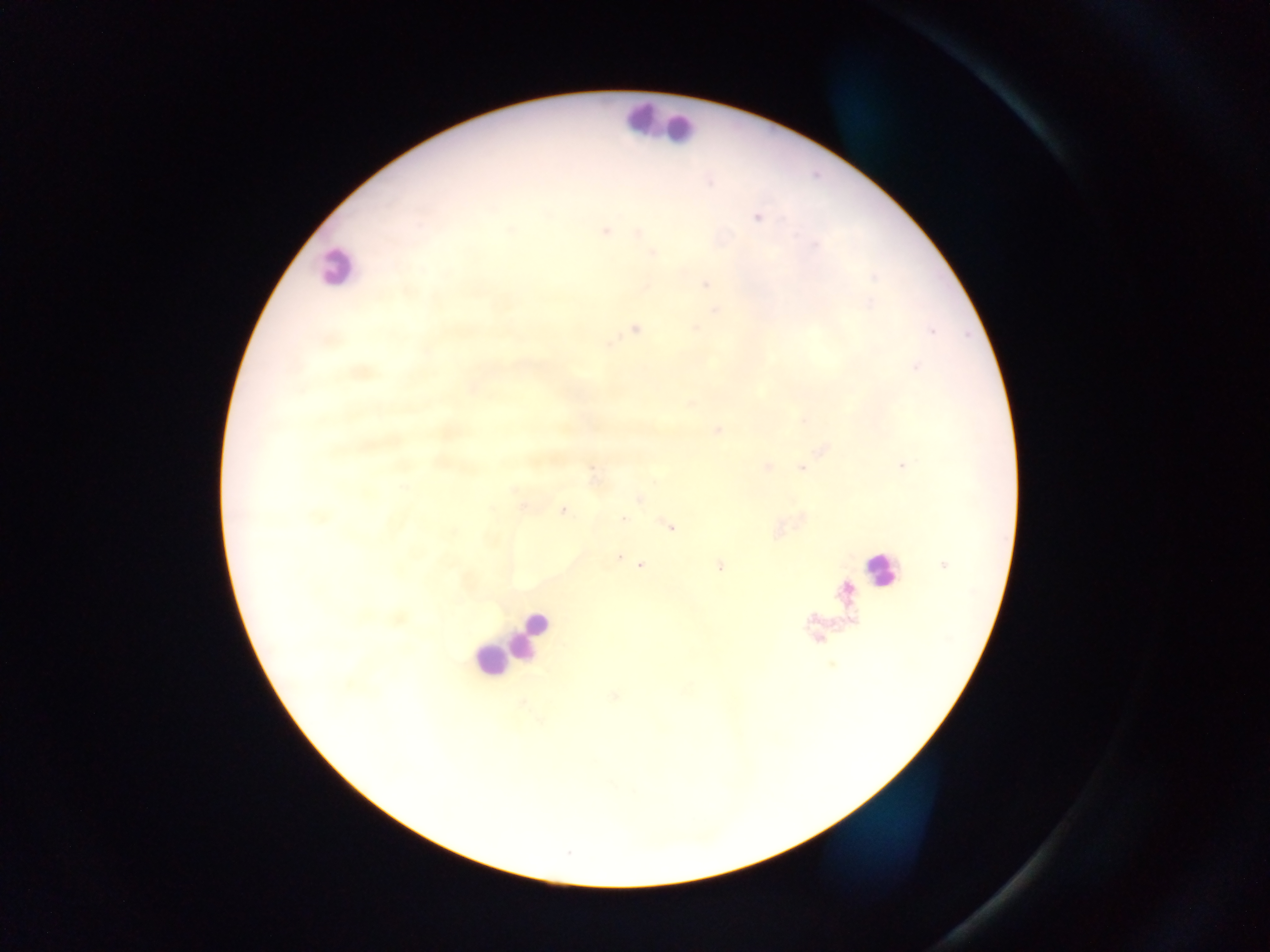
Approximate centers as {x, y} in pixels. Malaria parasite locations: {757, 217}, {510, 229}, {605, 231}, {638, 233}, {653, 252}, {705, 284}, {714, 310}, {634, 328}, {694, 328}, {931, 329}, {916, 367}, {359, 372}, {471, 389}, {690, 404}, {717, 430}, {822, 448}, {438, 462}, {901, 465}, {766, 467}, {801, 468}, {593, 475}, {640, 499}, {523, 504}, {563, 510}, {622, 519}, {669, 526}, {777, 530}, {618, 557}, {638, 562}, {639, 565}, {719, 565}, {944, 565}, {818, 638}, {613, 695}. Leukocyte locations: {659, 121}, {674, 126}, {336, 267}, {881, 569}, {536, 622}, {529, 633}, {513, 637}, {493, 658}. Thick blood smear. Collected in Ghana. Image is 1270×952 pixels. Photographed through a microscope with a mobile-phone camera. Single field of view.